Classify this cell by malaria status.
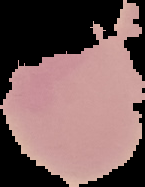

It is uninfected.

Summary:
  - Image size: 145×187 pixels
  - Image type: segmented cell region on a black background
  - Preparation: thin blood smear